Report the malaria status of this cell.
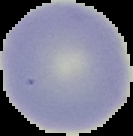

It is uninfected.

image size = 133×136 pixels
image type = segmented cell region on a black background
preparation = thin blood film